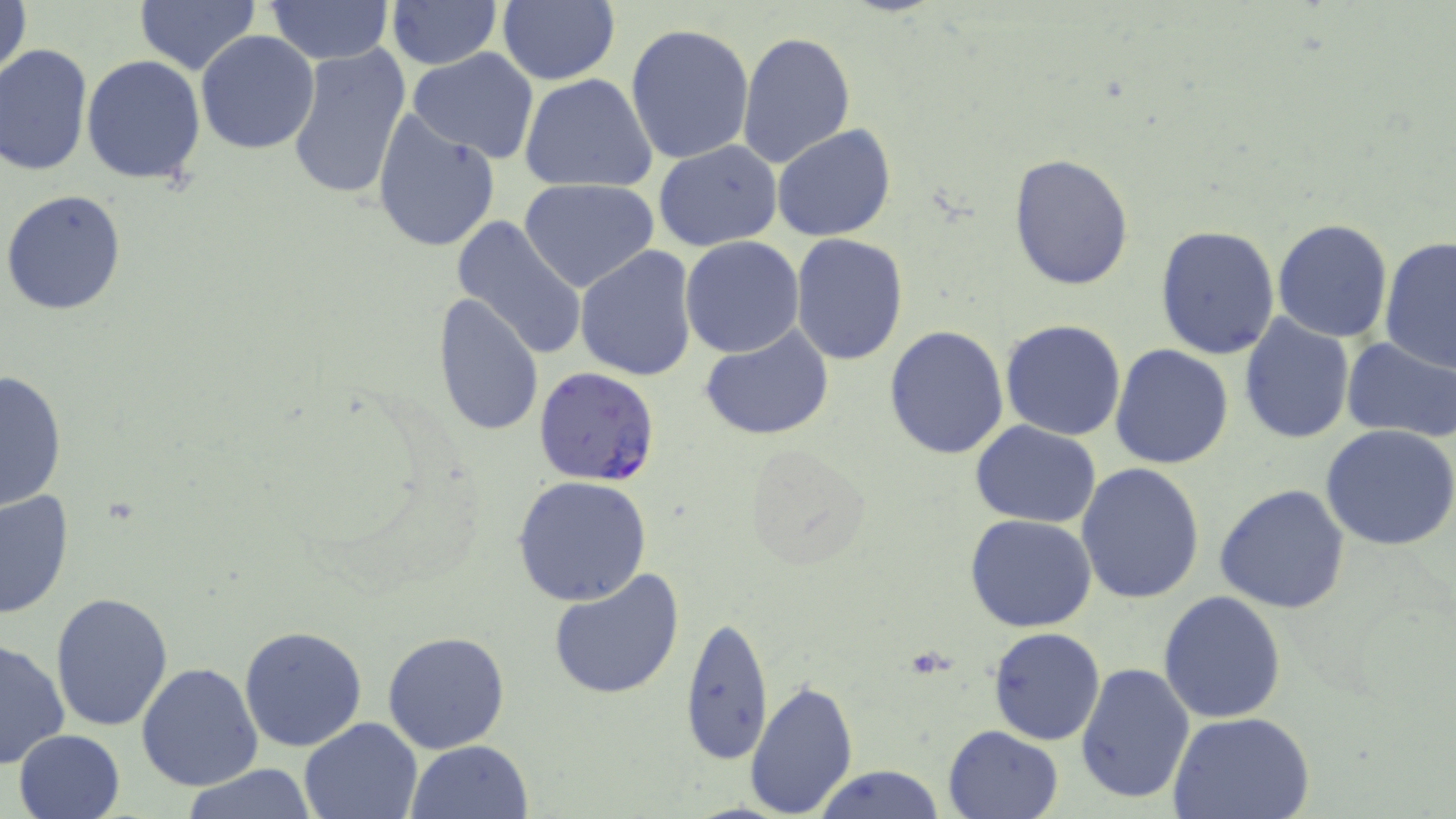
Approximate bounding boxes as (x1,y1)-(x2,y2) corner pairs in pixels. Uninfected red blood cell locations: (1,0)-(32,89), (135,0)-(259,75), (496,0)-(619,85), (264,1)-(396,64), (387,1)-(499,72), (624,22)-(755,165), (737,30)-(855,170), (195,31)-(321,154), (1,44)-(92,178), (287,44)-(411,203), (407,47)-(541,163), (81,55)-(207,186), (520,73)-(659,192), (370,106)-(502,254), (772,126)-(895,243), (653,141)-(783,252), (1008,153)-(1136,291), (519,178)-(661,293), (1,190)-(127,316), (451,217)-(588,360), (1271,218)-(1393,342), (1154,225)-(1282,361), (789,234)-(910,365), (679,236)-(804,358), (1376,236)-(1456,375), (574,245)-(699,381), (431,293)-(544,438), (1238,313)-(1356,445), (1000,319)-(1128,441), (700,324)-(835,442), (882,324)-(1010,460), (1342,337)-(1456,444), (1110,343)-(1235,469), (0,370)-(69,511), (971,421)-(1101,527), (1321,425)-(1456,552), (743,443)-(875,570), (1076,462)-(1205,604), (512,476)-(655,608), (1213,484)-(1352,614), (0,488)-(74,622), (965,514)-(1097,633), (547,569)-(685,701), (1159,590)-(1289,724), (49,591)-(174,733), (680,614)-(774,765), (239,626)-(368,751), (989,627)-(1107,746), (383,632)-(510,752), (0,638)-(71,771), (1075,661)-(1196,802), (137,662)-(264,792), (742,679)-(860,819), (1171,711)-(1315,819), (297,716)-(421,819), (943,725)-(1062,819), (14,730)-(125,818), (406,739)-(534,819), (811,763)-(947,819), (178,765)-(319,818). Plasmodium falciparum-infected red blood cell locations: (535,370)-(661,486). Slide-level diagnosis: Plasmodium falciparum. One field of a larger specimen. Light microscopy. Thin blood film. May-Grünwald-Giemsa stain. 1000x magnification. Image is 1456×819 pixels.